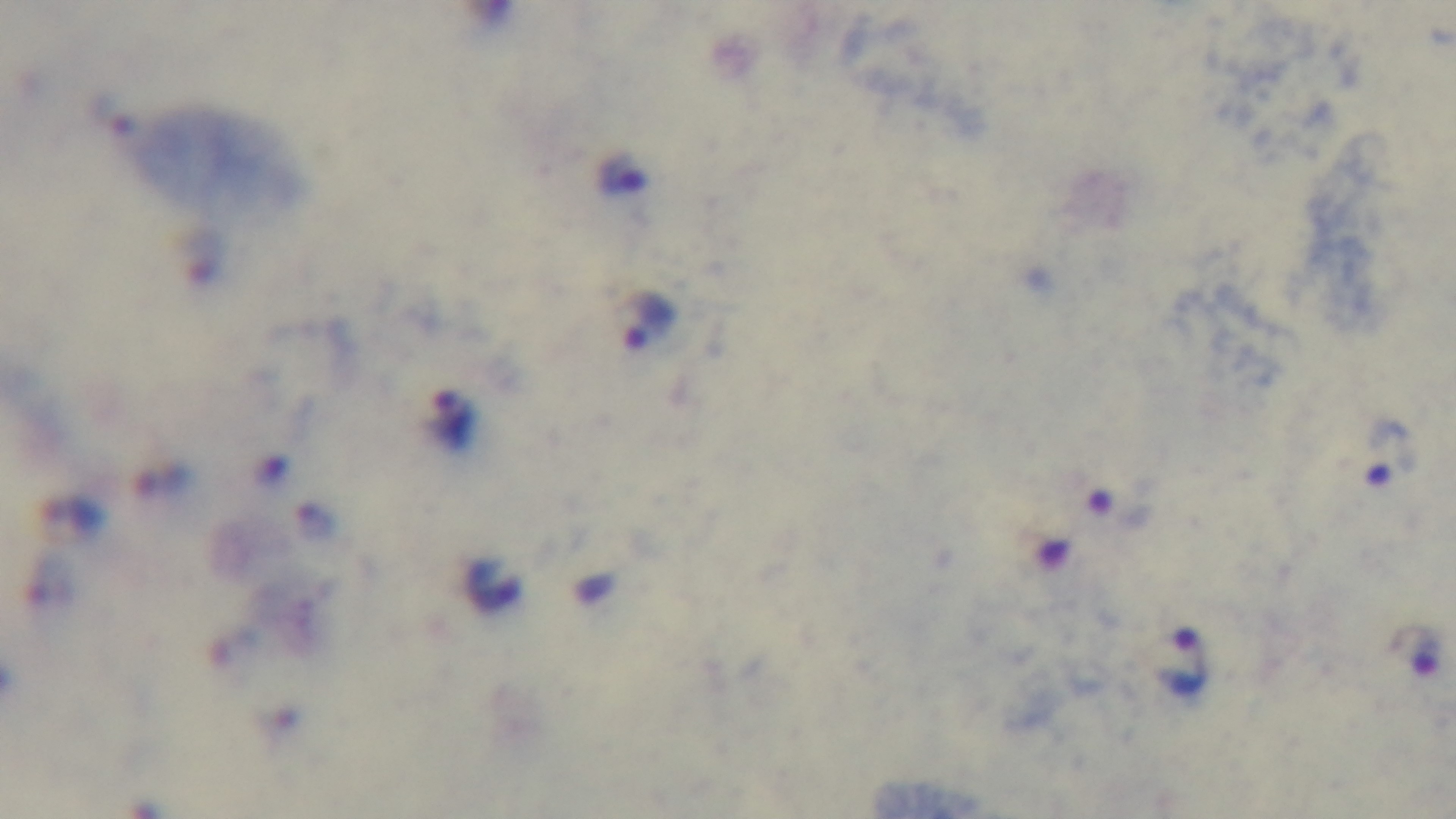
field of view = one from the slide
capture = mounted 4K digital camera
objective = 100x oil immersion
stain = Giemsa
preparation = thick
modality = light microscopy
malaria status = positive